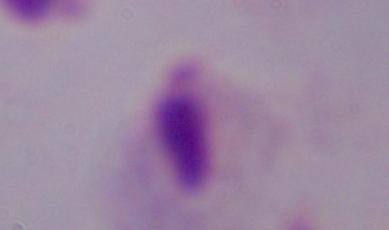 1000x magnification. A trichomonad is seen. Photomicrograph.